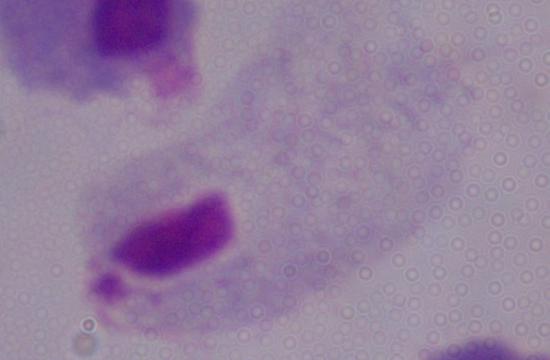 A trichomonad is shown. Micrograph. 1000x magnification.